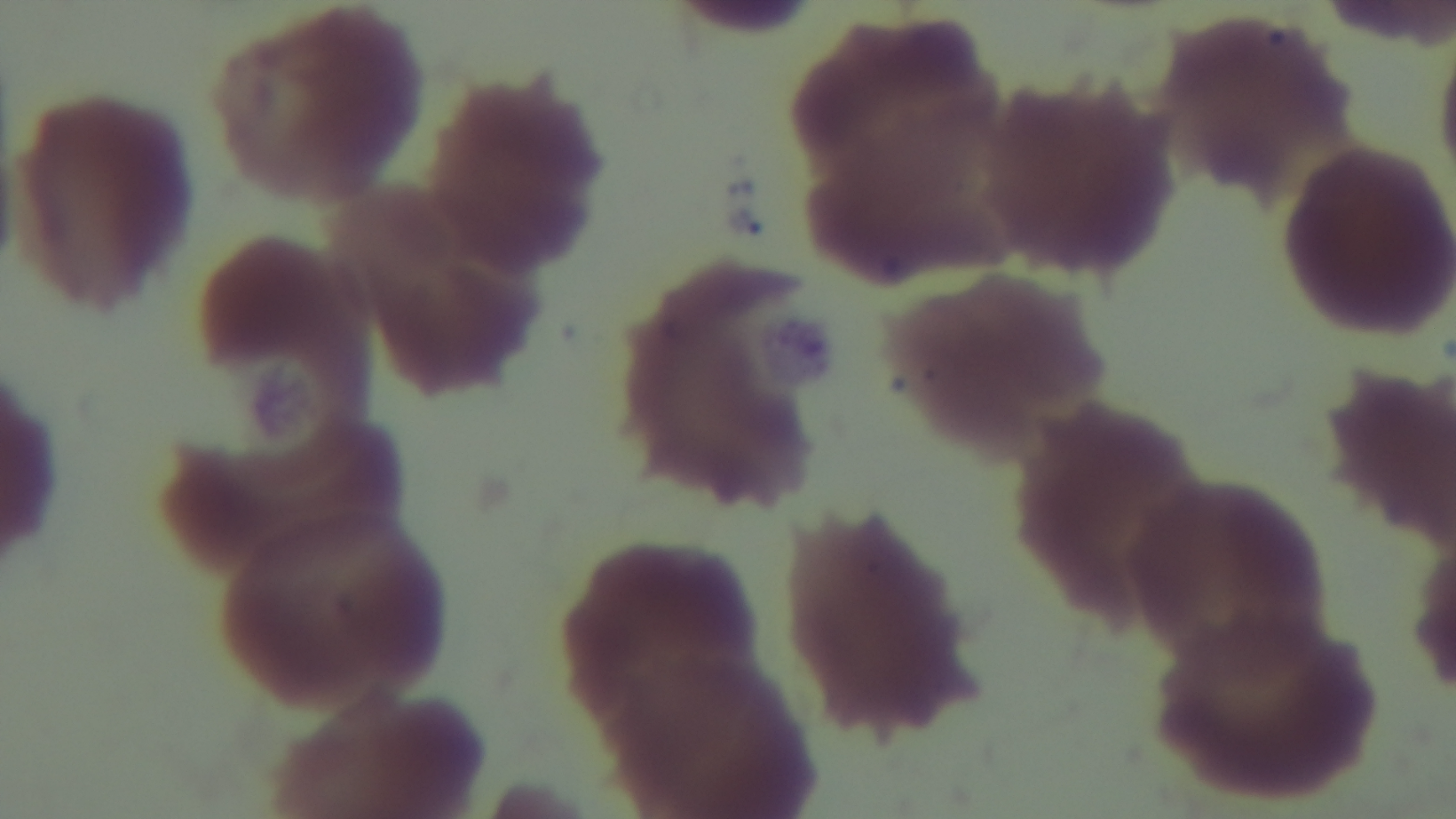
Summary:
  - Preparation: thin
  - Objective: 100x oil immersion
  - Capture: mounted 4K digital camera
  - Malaria status: negative
  - Field of view: one from the slide
  - Stain: Giemsa
  - Modality: light microscopy